Find the red blood cells that are infected with P. falciparum, and any of indeterminate infection status.
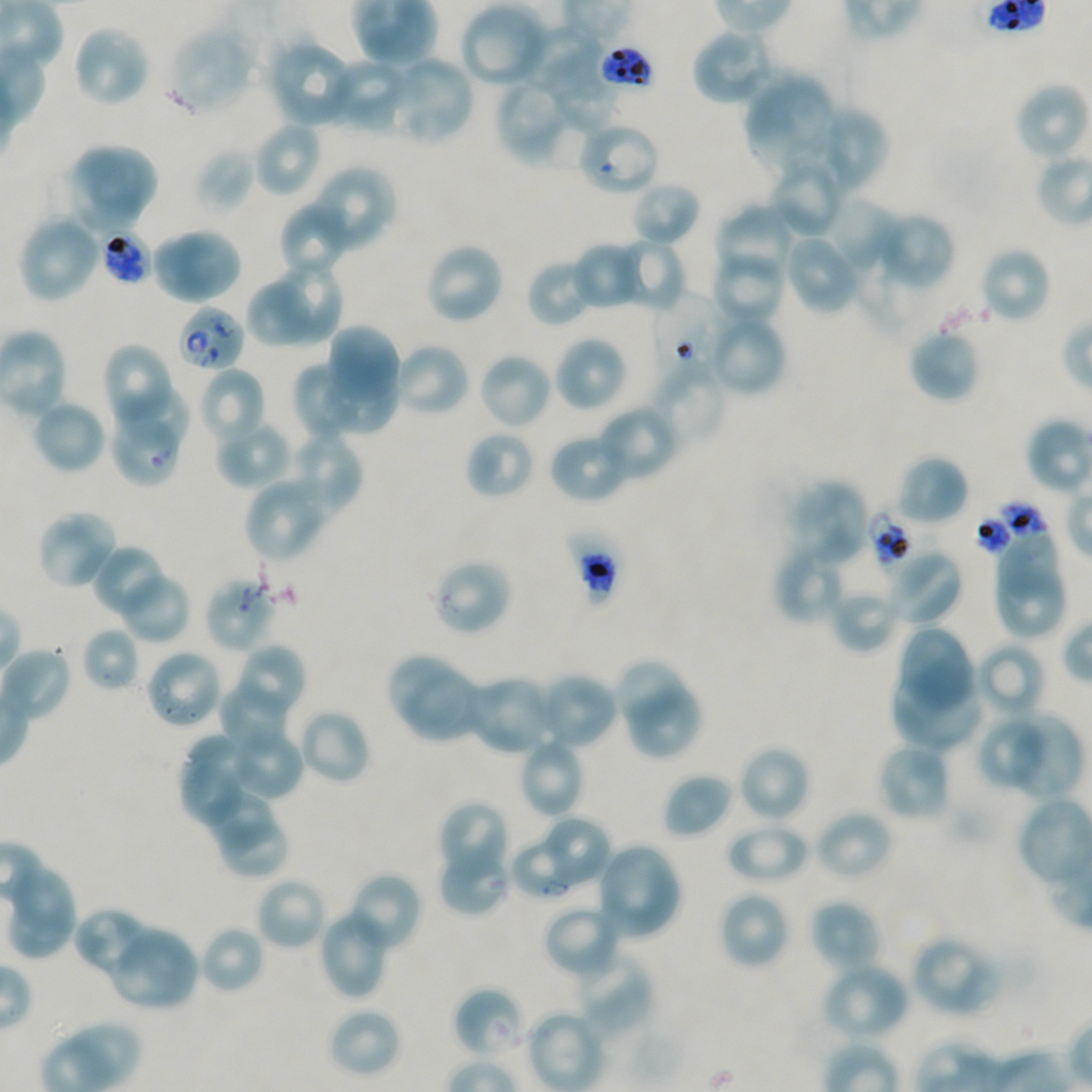
Approximate bounding boxes as {x1, y1, x2, y2} in pixels. Not every red blood cell is marked. A life-cycle stage — or a range of stages, where the recorded stages span more than one — follows each staged infected red blood cell.
Infected red blood cells: {98, 229, 151, 287} late trophozoite to late schizont; {177, 304, 245, 372}; {510, 837, 569, 896} ring.
Red blood cells of indeterminate infection status: {598, 43, 656, 92}, {582, 128, 657, 189}, {653, 295, 729, 377}, {110, 422, 179, 484}, {974, 499, 1053, 560}, {868, 509, 917, 576}, {563, 528, 623, 608}, {431, 558, 513, 636}, {204, 577, 275, 653}, {452, 986, 526, 1059}.

Summary:
  - Locations of uninfected red blood cells: {458, 2, 549, 89}, {72, 24, 151, 109}, {520, 24, 601, 92}, {170, 27, 255, 115}, {690, 27, 778, 107}, {271, 43, 350, 126}, {386, 58, 472, 139}, {333, 59, 408, 129}, {549, 67, 619, 134}, {744, 73, 838, 177}, {494, 77, 579, 166}, {1017, 81, 1089, 156}, {826, 105, 888, 194}, {253, 122, 321, 198}, {81, 143, 158, 212}, {195, 147, 255, 213}, {66, 160, 142, 235}, {312, 165, 396, 244}, {770, 166, 845, 238}, {631, 181, 701, 248}, {833, 198, 896, 270}, {279, 202, 349, 267}, {715, 205, 793, 275}, {875, 211, 956, 291}, {17, 214, 101, 303}, {170, 227, 243, 300}, {784, 232, 862, 315}, {615, 238, 686, 312}, {156, 240, 223, 303}, {571, 240, 644, 311}, {424, 241, 505, 325}, {711, 251, 786, 325}, {983, 252, 1049, 319}, {526, 257, 596, 327}, {278, 263, 344, 345}, {247, 278, 311, 348}, {715, 319, 784, 390}, {330, 324, 401, 388}, {908, 328, 980, 403}, {553, 335, 628, 414}, {101, 342, 172, 426}, {395, 346, 467, 414}, {481, 357, 550, 425}, {648, 359, 728, 448}, {297, 361, 357, 436}, {319, 365, 399, 432}, {204, 370, 264, 439}, {122, 385, 188, 445}, {35, 403, 106, 471}, {600, 410, 674, 480}, {219, 425, 293, 490}, {291, 429, 362, 511}, {465, 431, 534, 500}, {550, 439, 625, 500}, {895, 454, 969, 526}, {788, 479, 871, 567}, {248, 483, 315, 560}, {40, 513, 115, 585}, {1000, 528, 1060, 598}, {774, 541, 849, 626}, {95, 547, 162, 612}, {884, 547, 964, 627}, {996, 568, 1064, 637}, {117, 572, 192, 643}, {830, 587, 903, 654}, {896, 625, 975, 713}, {81, 627, 140, 693}, {975, 642, 1047, 720}, {239, 647, 303, 714}, {5, 649, 70, 719}, {150, 655, 221, 725}, {389, 656, 465, 730}, {615, 660, 682, 723}, {891, 661, 981, 752}, {404, 671, 477, 742}, {475, 678, 550, 754}, {539, 678, 613, 747}, {218, 685, 287, 753}, {630, 685, 703, 759}, {297, 708, 372, 786}, {1004, 714, 1084, 800}, {978, 719, 1044, 785}, {185, 735, 251, 801}, {226, 735, 303, 802}, {876, 742, 951, 823}, {523, 743, 582, 817}, {737, 744, 811, 824}, {179, 761, 242, 829}, {662, 773, 733, 839}, {209, 794, 274, 850}, {440, 803, 506, 876}, {814, 809, 894, 882}, {549, 818, 609, 884}, {725, 820, 809, 885}, {224, 821, 286, 875}, {600, 848, 678, 936}, {439, 854, 509, 915}, {12, 869, 74, 931}, {354, 876, 417, 946}, {259, 881, 323, 947}, {718, 890, 790, 970}, {810, 899, 883, 974}, {8, 905, 77, 959}, {322, 907, 385, 997}, {73, 909, 151, 974}, {546, 911, 615, 975}, {199, 925, 265, 994}, {111, 931, 196, 1005}, {911, 934, 1000, 1018}, {582, 953, 653, 1029}, {820, 961, 911, 1042}, {327, 1007, 402, 1078}
  - Stain: Giemsa
  - Culture: static in-vitro P. falciparum strain NF54
  - Donor blood group: A+/O+
  - Field of view: one from this slide
  - Objective: 100x, oil immersion, numerical aperture 1.45
  - Image size: 1092×1092 pixels
  - Preparation: thin blood film